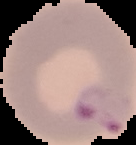
Summary:
  - Image type: segmented cell region with the area outside set to black
  - Malaria status: parasitized
  - Preparation: thin blood film
  - Image size: 136×145 pixels